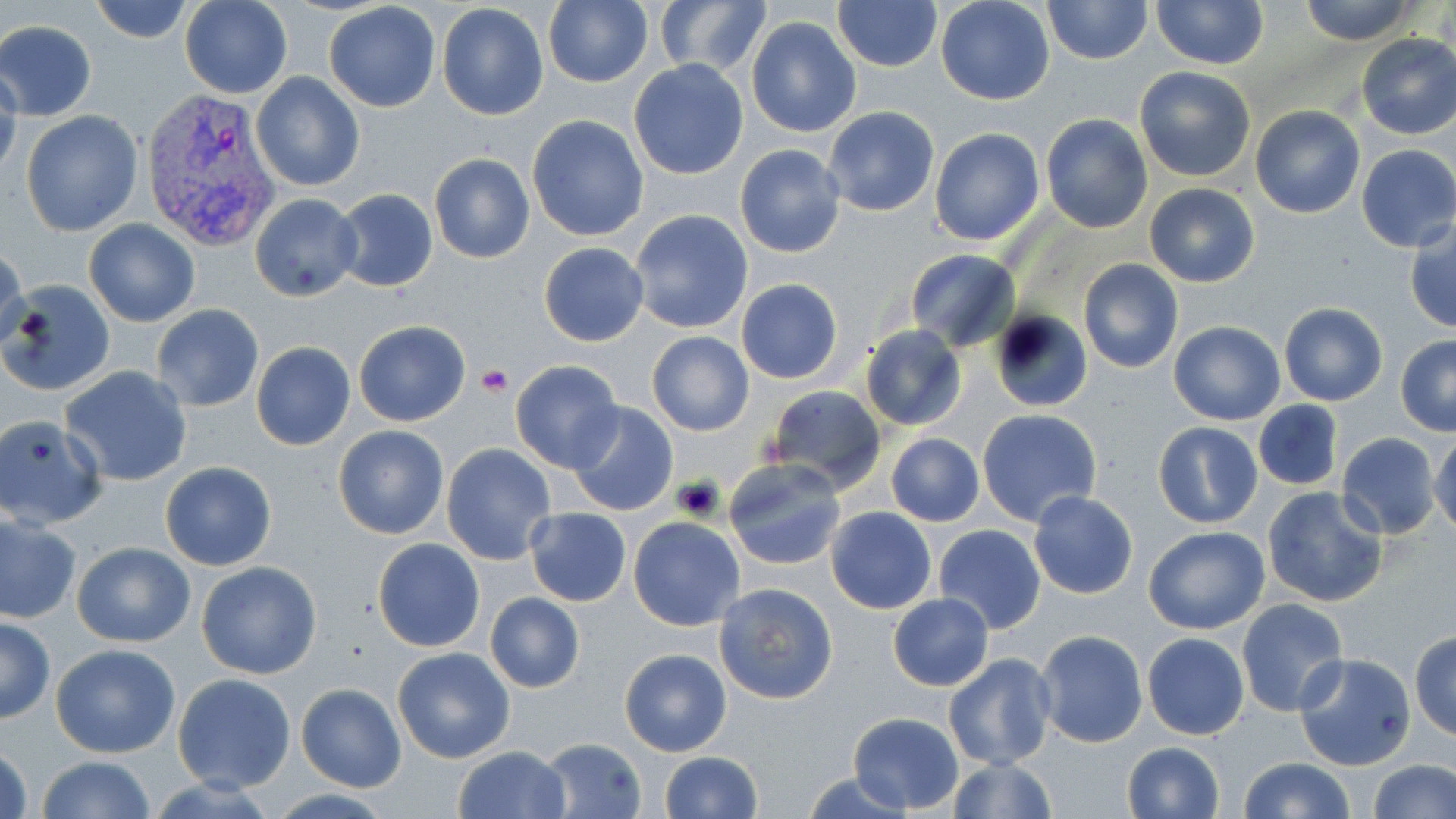
Summary:
  - Coordinate format: approximate bounding boxes as [x1, y1, x2, y2] in pixels
  - Uninfected red blood cell locations: [89, 0, 195, 44], [935, 0, 1055, 105], [1042, 0, 1153, 66], [1298, 0, 1420, 45], [179, 1, 292, 98], [436, 1, 550, 122], [655, 1, 771, 78], [831, 1, 942, 71], [1150, 1, 1270, 70], [323, 2, 441, 113], [542, 2, 653, 87], [746, 15, 862, 138], [0, 19, 99, 119], [1356, 32, 1456, 140], [628, 59, 749, 180], [1133, 65, 1257, 182], [0, 68, 22, 185], [252, 72, 364, 192], [1249, 105, 1365, 218], [823, 106, 940, 217], [21, 110, 144, 237], [1040, 113, 1153, 233], [527, 114, 649, 241], [929, 127, 1045, 246], [1356, 143, 1456, 252], [735, 144, 845, 258], [428, 154, 535, 264], [1144, 183, 1260, 287], [331, 190, 438, 294], [250, 192, 363, 302], [628, 209, 754, 334], [83, 218, 200, 326], [1405, 219, 1456, 333], [538, 242, 648, 347], [1, 244, 27, 356], [904, 249, 1020, 351], [1078, 258, 1184, 373], [2, 279, 117, 399], [735, 279, 844, 384], [1279, 303, 1387, 406], [151, 304, 266, 413], [989, 310, 1092, 413], [353, 320, 469, 426], [1168, 320, 1285, 425], [860, 325, 966, 431], [646, 331, 754, 435], [1395, 335, 1456, 435], [252, 342, 355, 451], [510, 360, 625, 473], [61, 365, 192, 487], [764, 384, 885, 495], [1254, 401, 1343, 489], [567, 402, 678, 516], [977, 408, 1103, 527], [0, 415, 107, 531], [1154, 421, 1262, 528], [333, 425, 451, 540], [1431, 426, 1456, 536], [1336, 432, 1444, 540], [885, 433, 985, 527], [442, 444, 558, 565], [723, 458, 848, 571], [159, 461, 277, 571], [1262, 486, 1389, 608], [1029, 491, 1138, 599], [826, 506, 936, 614], [526, 509, 631, 605], [0, 512, 80, 625], [628, 518, 744, 631], [934, 524, 1046, 634], [1143, 526, 1270, 635], [373, 538, 484, 652], [71, 541, 195, 647], [195, 561, 323, 680], [714, 581, 838, 703], [484, 592, 584, 692], [887, 593, 995, 691], [1237, 600, 1351, 718], [0, 617, 54, 723], [1034, 630, 1147, 748], [1410, 630, 1456, 741], [1142, 633, 1251, 740], [50, 643, 181, 758], [393, 646, 515, 763], [619, 648, 732, 756], [1293, 652, 1417, 771], [944, 653, 1056, 770], [171, 673, 297, 793], [296, 683, 406, 792], [847, 711, 962, 814], [539, 738, 647, 818], [1121, 741, 1225, 819], [1, 742, 33, 819], [452, 745, 572, 819], [658, 751, 762, 819], [33, 755, 157, 819], [946, 756, 1058, 819], [1237, 758, 1355, 818], [1367, 758, 1454, 818], [802, 772, 917, 818]
  - Plasmodium vivax-infected red blood cell locations: [141, 88, 284, 250]
  - Platelet locations: [476, 365, 511, 396], [673, 475, 725, 521]
  - Slide-level diagnosis: Plasmodium vivax
  - Magnification: 1000x
  - Modality: light microscopy
  - Field of view: one of a larger specimen
  - Stain: May-Grünwald-Giemsa
  - Image size: 1456×819 pixels
  - Preparation: thin blood film